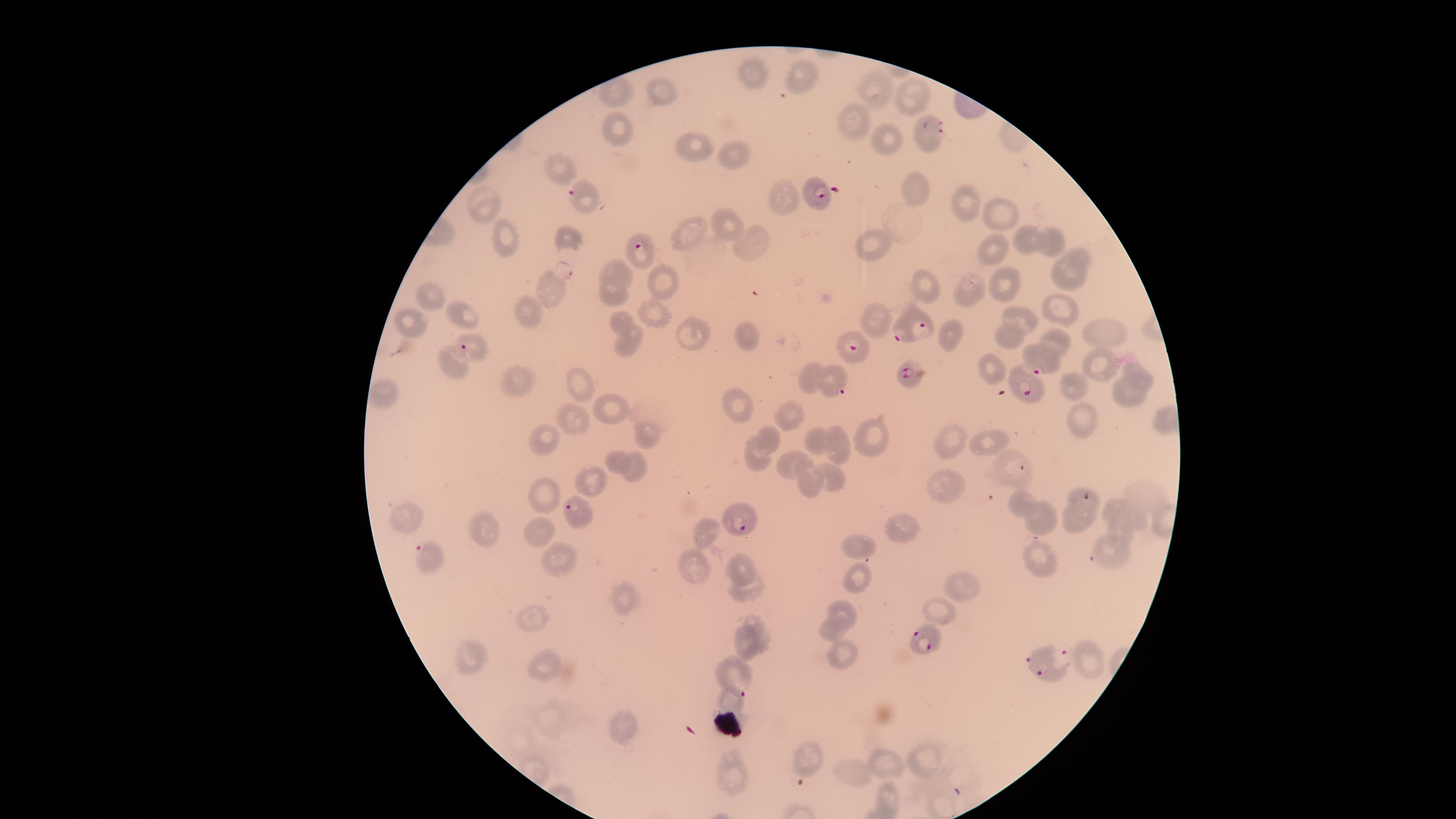
stain = Giemsa
species = Plasmodium falciparum
uninfected red blood cells = approximate marker points as (x, y) in pixels: (757, 76), (803, 81), (661, 92), (905, 92), (614, 93), (876, 93), (851, 121), (614, 129), (885, 136), (689, 148), (737, 152), (560, 170), (915, 185), (781, 199), (965, 199), (482, 203), (995, 211), (734, 227), (687, 232), (565, 237), (1025, 239), (1056, 240), (506, 243), (752, 245), (874, 247), (991, 253), (1082, 253), (611, 269), (1068, 275), (665, 281), (1004, 286), (923, 288), (548, 289), (965, 289), (610, 296), (435, 299), (1058, 309), (465, 313), (530, 314), (648, 316), (1024, 316), (615, 318), (415, 320), (873, 320), (1102, 328), (950, 334), (1006, 336), (1057, 337), (696, 341), (744, 341), (631, 348), (1102, 365), (452, 367), (992, 367), (817, 376), (1144, 376), (519, 384), (1074, 385), (578, 390), (382, 398), (1129, 398), (735, 406), (614, 409), (790, 417), (569, 423), (1080, 426), (652, 435), (875, 436), (837, 438), (540, 440), (769, 440), (954, 441), (988, 441), (812, 443), (619, 458), (760, 459), (790, 465), (1009, 467), (638, 470), (595, 481), (830, 483), (945, 484), (810, 486), (1145, 494), (550, 496), (1024, 499), (1115, 504), (406, 516), (1042, 518), (1078, 526), (1118, 527), (540, 529), (898, 530), (707, 531), (486, 532), (862, 543), (1113, 547), (561, 556), (1037, 557), (743, 564), (693, 571), (862, 580), (754, 587), (965, 588), (622, 600), (842, 609), (943, 612), (535, 620), (830, 627), (748, 635), (844, 651), (467, 661), (1090, 662), (546, 665), (730, 700), (623, 729), (805, 756), (928, 759), (889, 767), (853, 773), (732, 777), (886, 797)
visible region = circular
capture = smartphone photograph through the microscope eyepiece
parasitized red blood cells = approximate marker points as (x, y) in pixels: (929, 130), (580, 194), (819, 200), (639, 251), (910, 326), (853, 349), (469, 352), (1040, 358), (910, 377), (832, 383), (1029, 394), (1086, 498), (576, 512), (741, 519), (425, 557), (923, 641), (1049, 661), (731, 674)
presence = malaria parasites detected
image size = 1456×819 pixels
preparation = thin blood smear
field of view = single